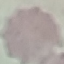
{
  "malaria_status": "uninfected",
  "stain": "Giemsa",
  "image_type": "cell patch, automatically extracted from a larger field of view and resized to 64 × 64 pixels",
  "capture": "smartphone through the microscope eyepiece",
  "preparation": "thin blood smear"
}